Classify this cell by malaria status.
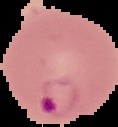
It is parasitized.

image size = 118×127 pixels
preparation = thin blood film
image type = segmented cell region with the area outside set to black